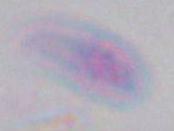 1000x magnification. Micrograph. Toxoplasma gondii is shown.